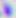
Summary:
  - Identification: Toxoplasma gondii
  - Modality: micrograph
  - Magnification: 400x